Assess this cell for malaria.
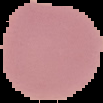
It is uninfected.

Summary:
  - Image size: 103×103 pixels
  - Preparation: thin blood smear
  - Image type: segmented cell region on a black background